Assess this cell for malaria.
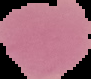

Uninfected.

image type = segmented cell region on a black background
image size = 91×79 pixels
preparation = thin blood smear